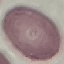
malaria status = uninfected
preparation = thin smear
image type = cell patch, automatically extracted from a larger field of view and resized to 64 × 64 pixels
capture = smartphone through the microscope eyepiece
stain = Giemsa